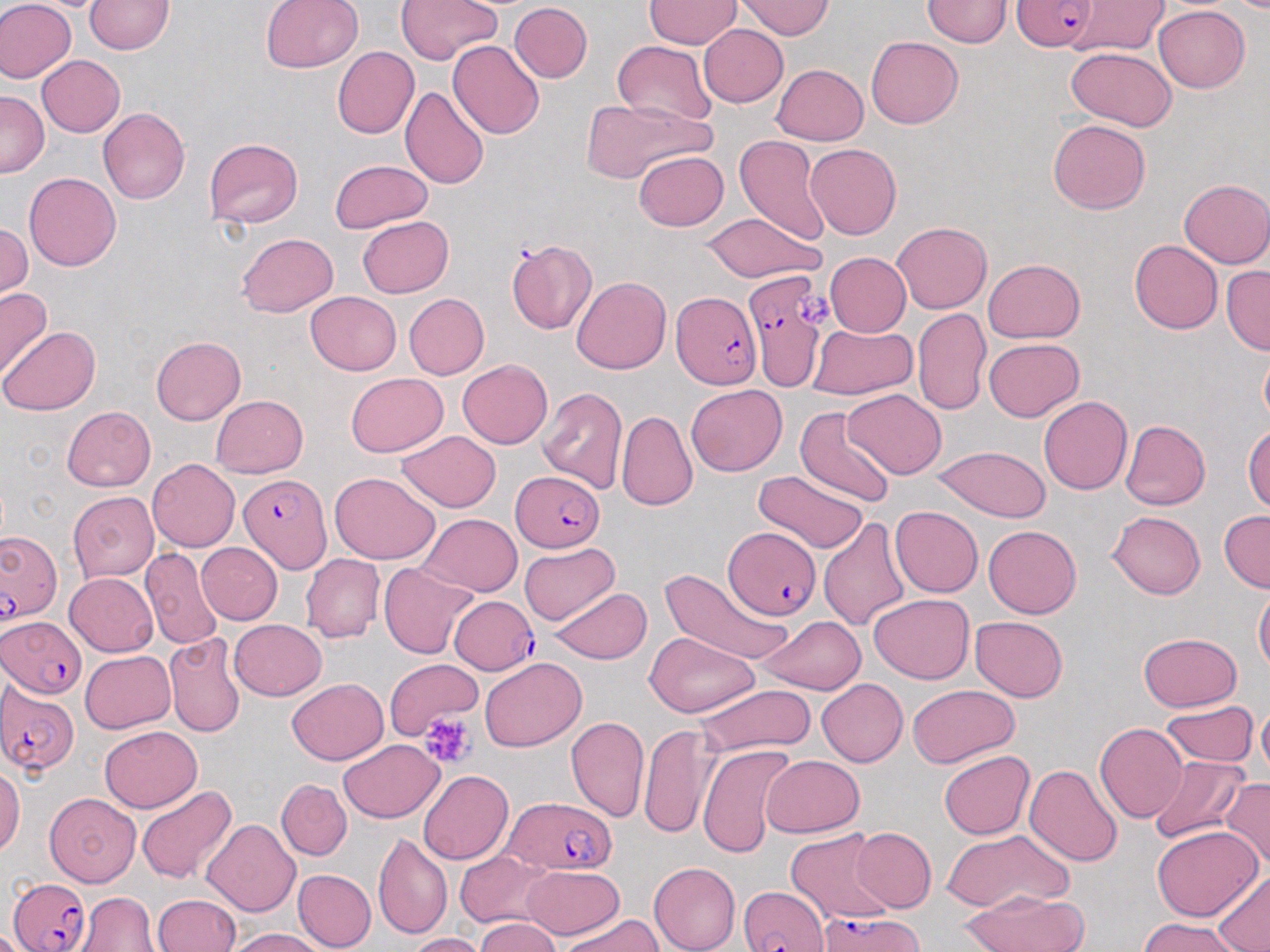

slide-level diagnosis = Plasmodium falciparum
platelet locations = approximate bounding boxes as (x1, y1, x2, y2) in pixels: (799, 290, 836, 329), (419, 712, 476, 770)
stain = May-Grünwald-Giemsa
image size = 1270×952 pixels
modality = light microscopy
magnification = 1000x
Plasmodium falciparum-infected red blood cell locations = approximate bounding boxes as (x1, y1, x2, y2) in pixels: (1012, 0, 1099, 52), (742, 274, 829, 392), (672, 291, 762, 388), (510, 470, 605, 552), (238, 474, 332, 573), (723, 526, 821, 620), (1, 532, 62, 625), (449, 594, 538, 675), (1, 615, 86, 698), (0, 681, 80, 777), (501, 795, 612, 875), (10, 877, 92, 951), (739, 884, 831, 952), (817, 909, 921, 952)
preparation = thin blood smear
uninfected red blood cell locations = approximate bounding boxes as (x1, y1, x2, y2) in pixels: (0, 0, 76, 83), (260, 0, 364, 74), (398, 0, 501, 63), (644, 0, 740, 48), (1067, 0, 1171, 54), (85, 1, 175, 54), (735, 1, 834, 39), (922, 1, 1011, 47), (509, 3, 592, 82), (1154, 5, 1249, 92), (698, 24, 788, 107), (867, 36, 963, 128), (447, 40, 545, 139), (613, 41, 716, 128), (333, 46, 418, 139), (1065, 47, 1177, 131), (37, 55, 125, 136), (773, 64, 868, 145), (399, 86, 490, 190), (1, 90, 48, 177), (580, 97, 711, 185), (99, 108, 190, 204), (1047, 119, 1151, 215), (735, 135, 829, 245), (203, 138, 302, 228), (805, 143, 902, 240), (634, 150, 728, 230), (329, 159, 433, 234), (24, 173, 121, 272), (1178, 178, 1270, 268), (702, 212, 824, 283), (358, 216, 453, 297), (892, 222, 991, 314), (0, 223, 32, 300), (235, 233, 339, 318), (506, 238, 596, 334), (1129, 239, 1222, 333), (824, 252, 911, 336), (983, 259, 1085, 343), (1221, 265, 1270, 355), (571, 276, 671, 374), (0, 287, 53, 382), (306, 292, 401, 374), (404, 294, 488, 380), (913, 307, 990, 415), (808, 323, 918, 398), (1, 326, 99, 415), (151, 335, 245, 425), (983, 337, 1084, 422), (1260, 350, 1270, 427), (457, 359, 552, 449), (346, 372, 448, 456), (687, 384, 786, 476), (536, 385, 627, 495), (842, 388, 946, 479), (211, 395, 307, 477), (1038, 396, 1132, 496), (63, 406, 155, 492), (794, 407, 898, 508), (616, 410, 697, 511), (1121, 419, 1210, 510), (1243, 425, 1270, 514), (397, 430, 501, 512), (932, 445, 1051, 521), (148, 459, 240, 551), (752, 469, 867, 554), (329, 471, 441, 565), (68, 493, 159, 582), (890, 506, 983, 597), (1218, 510, 1270, 593), (1108, 511, 1205, 599), (418, 514, 523, 596), (818, 517, 911, 631), (982, 524, 1081, 618), (197, 543, 282, 624), (517, 543, 619, 626), (139, 547, 223, 649), (300, 554, 385, 643), (379, 562, 478, 659), (660, 567, 793, 668), (65, 572, 158, 657), (1253, 584, 1270, 677), (548, 587, 651, 664), (869, 593, 973, 684), (758, 615, 867, 695), (970, 616, 1068, 702), (230, 619, 326, 700), (645, 631, 760, 719), (1137, 632, 1243, 711), (164, 633, 247, 737), (81, 650, 176, 733), (479, 655, 586, 752), (385, 657, 482, 738), (286, 679, 389, 765), (816, 679, 907, 766), (693, 684, 816, 758), (908, 685, 1019, 767), (1257, 697, 1270, 787), (1160, 701, 1257, 768), (566, 715, 650, 823), (99, 724, 202, 812), (638, 724, 717, 842), (1094, 724, 1187, 823), (338, 740, 445, 823), (698, 743, 800, 860), (938, 750, 1035, 839), (760, 755, 865, 836), (1148, 756, 1251, 845), (1025, 763, 1124, 867), (0, 766, 25, 856), (418, 770, 512, 865), (276, 779, 351, 860), (1219, 779, 1270, 872), (135, 786, 238, 886), (45, 792, 141, 886), (201, 819, 298, 917), (1152, 825, 1262, 921), (851, 827, 936, 911), (784, 828, 895, 924), (941, 828, 1073, 915), (373, 831, 452, 941), (454, 850, 553, 928), (648, 862, 740, 952), (520, 865, 623, 938), (292, 869, 377, 952), (1212, 869, 1270, 951), (957, 890, 1089, 952), (76, 892, 160, 951), (152, 894, 241, 952), (559, 914, 663, 952), (1138, 916, 1245, 952), (474, 917, 563, 952), (225, 927, 330, 951), (405, 932, 488, 952)
field of view = one of a larger specimen